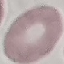
Summary:
  - Result: no malaria parasites detected
  - Capture: smartphone through the microscope eyepiece
  - Stain: Giemsa
  - Preparation: thin smear
  - Image type: cell patch, automatically extracted from a larger field of view and resized to 64 × 64 pixels